Identify the blood parasite species.
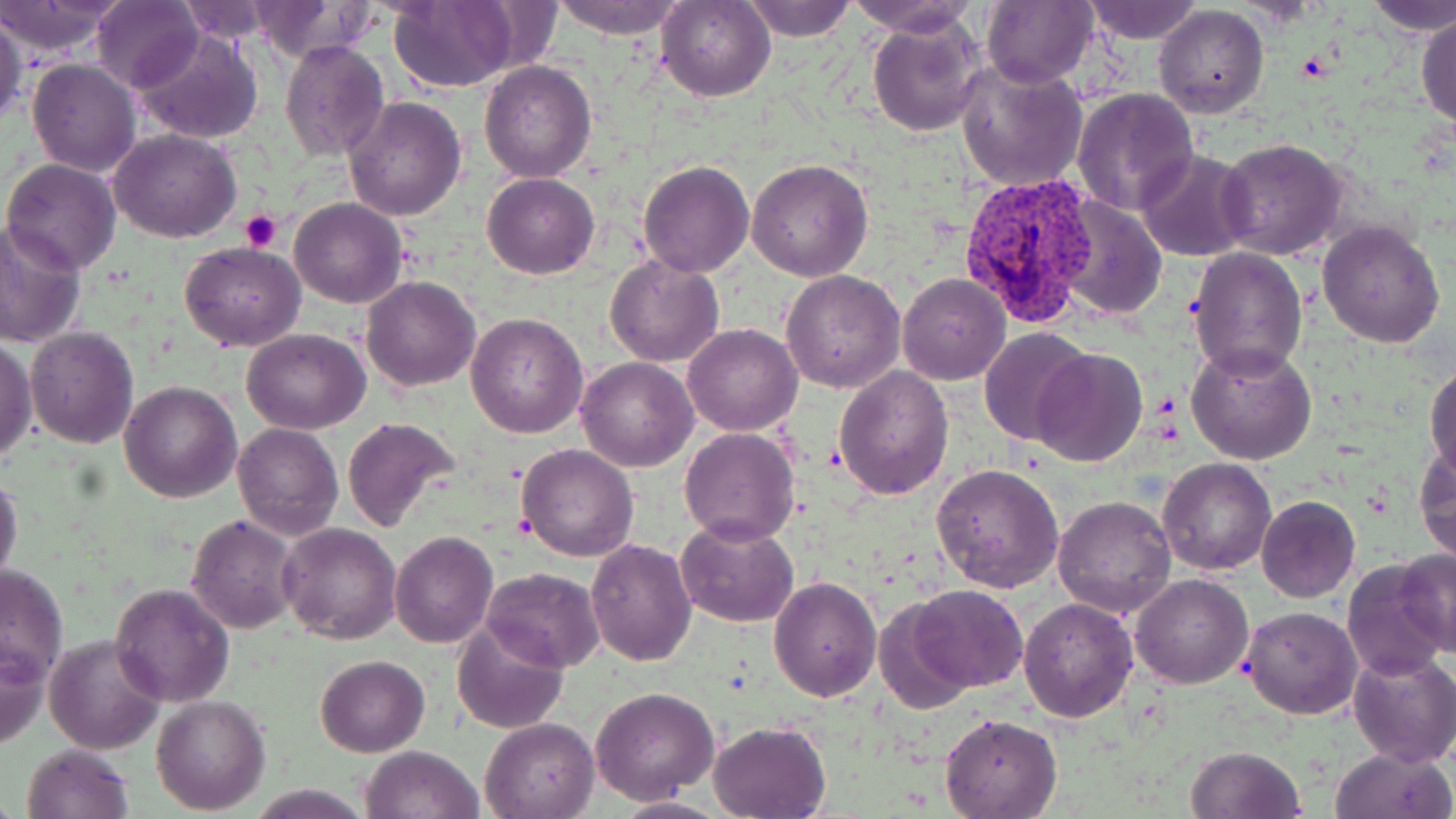

Plasmodium vivax.

Approximate bounding boxes as (x1,y1)-(x2,y2) corner pairs in pixels. Plasmodium vivax-infected red blood cell locations: (957,170)-(1098,328). Platelet locations: (241,209)-(282,253). Uninfected red blood cell locations: (0,0)-(123,58), (250,0)-(376,59), (549,0)-(689,37), (742,0)-(855,42), (849,0)-(979,37), (1082,0)-(1203,44), (1362,0)-(1456,37), (92,1)-(202,93), (388,1)-(522,91), (657,1)-(775,101), (981,2)-(1096,87), (178,3)-(275,42), (1154,5)-(1268,117), (0,7)-(24,130), (1417,12)-(1456,131), (867,21)-(984,137), (133,28)-(261,144), (280,40)-(388,161), (27,57)-(141,176), (956,59)-(1089,192), (480,61)-(597,183), (1072,87)-(1200,214), (343,98)-(466,221), (110,129)-(240,242), (1217,137)-(1349,261), (1136,149)-(1254,261), (3,158)-(122,273), (747,159)-(873,280), (638,161)-(754,277), (482,172)-(599,278), (1054,194)-(1168,318), (289,198)-(408,309), (0,219)-(88,350), (1317,220)-(1447,347), (180,241)-(306,351), (1186,245)-(1308,381), (606,254)-(723,367), (781,271)-(905,392), (897,273)-(1011,384), (362,276)-(480,391), (467,312)-(588,438), (683,323)-(802,435), (24,326)-(138,447), (242,327)-(369,434), (978,327)-(1092,445), (0,337)-(36,466), (1188,340)-(1316,465), (1030,348)-(1147,467), (576,355)-(697,471), (1425,362)-(1456,481), (834,365)-(955,501), (119,380)-(242,502), (342,417)-(462,534), (232,423)-(343,539), (679,428)-(799,545), (516,443)-(640,562), (1416,446)-(1456,564), (1157,459)-(1276,575), (931,462)-(1064,593), (0,471)-(24,592), (1052,495)-(1177,617), (1255,496)-(1360,602), (186,514)-(304,634), (675,518)-(798,626), (277,523)-(401,645), (390,531)-(498,648), (585,538)-(697,667), (1394,545)-(1456,660), (1342,558)-(1449,683), (0,562)-(70,687), (481,567)-(604,673), (1131,574)-(1253,689), (769,575)-(881,702), (109,582)-(235,705), (910,585)-(1027,693), (1022,588)-(1252,704), (1020,598)-(1138,723), (873,600)-(978,713), (1241,606)-(1362,718), (453,618)-(568,735), (45,633)-(165,755), (1,636)-(48,751), (1349,650)-(1456,767), (316,655)-(430,756), (592,686)-(720,804), (151,694)-(271,813), (940,714)-(1061,818), (480,717)-(601,818), (708,720)-(832,818), (21,742)-(135,819), (362,746)-(483,819), (1185,746)-(1304,819), (1328,746)-(1455,819), (610,794)-(732,817). 1000x magnification. Light microscopy. Single field of view. Image is 1456×819 pixels. May-Grünwald-Giemsa stain. Thin blood smear.